Identify the parasite.
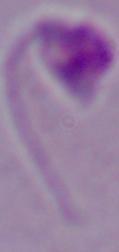
Leishmania.

{
  "magnification": "1000x",
  "modality": "photomicrograph"
}